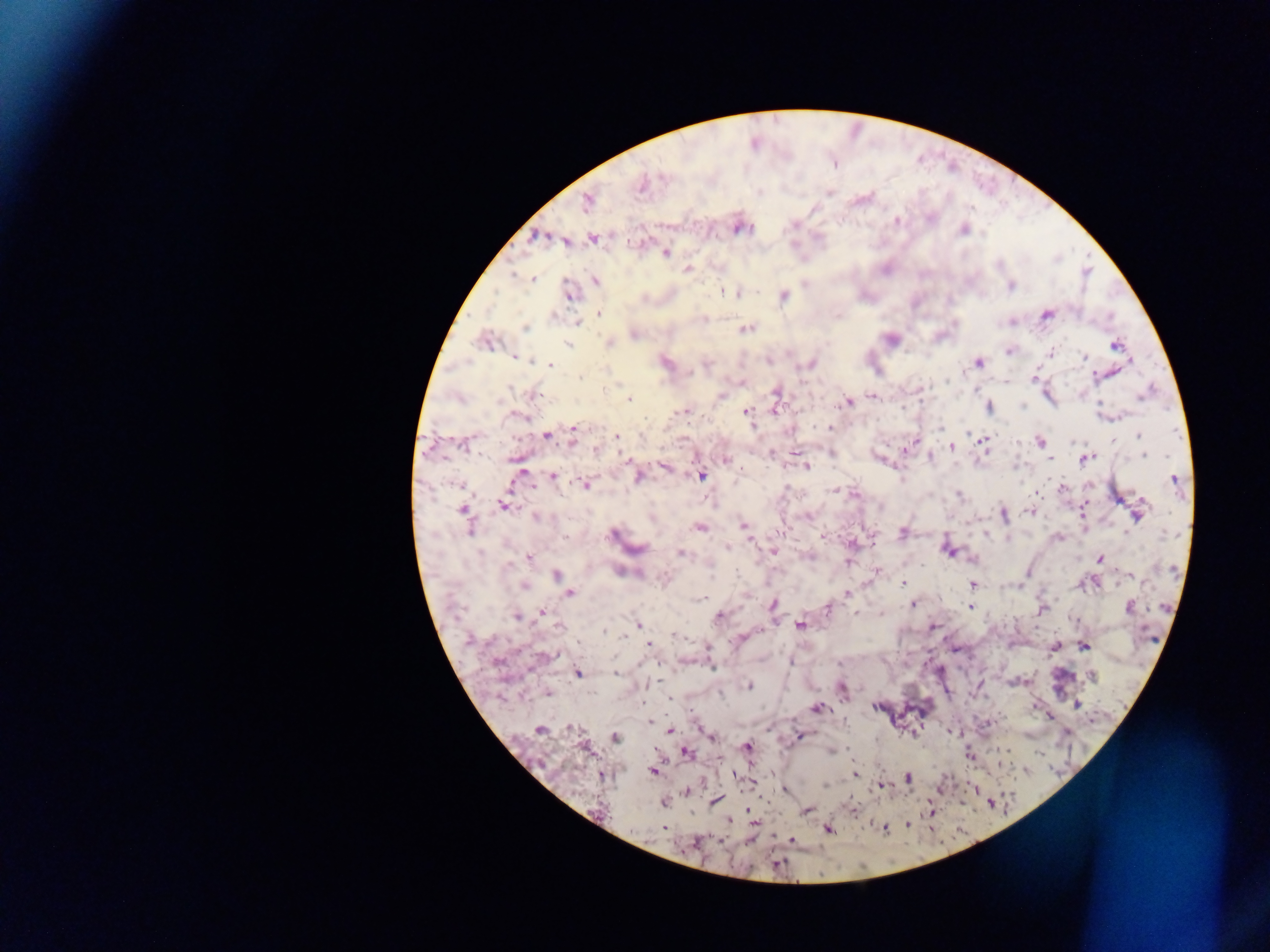
field_of_view: single
country: Ghana
capture: mobile-phone photograph through a microscope
preparation: thick blood smear
plasmodium_parasite_locations: 'approximate centers as (x, y) in pixels: (642, 184), (828, 192), (587, 200), (896, 221), (739, 226), (963, 229), (537, 237), (593, 238), (573, 239), (565, 241), (665, 253), (687, 269), (533, 279), (594, 281), (1010, 286), (569, 292), (737, 293), (782, 295), (598, 314), (1046, 314), (1010, 321), (577, 323), (526, 328), (744, 328), (634, 334), (890, 339), (486, 340), (608, 343), (566, 344), (1115, 345), (1010, 351), (1052, 352), (513, 356), (1084, 359), (664, 361), (977, 362), (810, 364), (551, 365), (1095, 375), (1035, 377), (777, 393), (531, 394), (720, 395), (873, 396), (629, 400), (847, 402), (987, 407), (774, 408), (684, 409), (746, 410), (517, 416), (828, 427), (573, 429), (547, 434), (1140, 434), (573, 437), (616, 438), (982, 440), (1039, 441), (464, 444), (904, 447), (950, 447), (595, 449), (830, 452), (772, 453), (1144, 455), (930, 456), (1085, 458), (726, 459), (806, 465), (665, 467), (520, 472), (701, 474), (637, 475), (552, 476), (1174, 479), (584, 484), (1061, 487), (836, 489), (854, 493), (958, 494), (503, 505), (464, 509), (1083, 509), (1030, 511), (1137, 513), (1002, 514), (808, 515), (537, 516), (653, 518), (744, 526), (700, 527), (470, 528), (902, 532), (613, 533), (822, 535), (986, 536), (1057, 537), (851, 543), (727, 546), (635, 548), (947, 549), (773, 551), (679, 553), (809, 556), (528, 557), (971, 558), (1100, 559), (849, 560), (624, 571), (876, 571), (557, 574), (1131, 575), (562, 581), (903, 582), (971, 584), (523, 586), (569, 592), (847, 593), (701, 599), (913, 604), (773, 605), (971, 606), (827, 607), (1129, 607), (1041, 609), (541, 613), (882, 613), (855, 614), (517, 616), (719, 616), (800, 624), (638, 625), (932, 626), (604, 630), (674, 635), (621, 636), (742, 637), (1083, 644), (649, 645), (1053, 646), (546, 656), (712, 667), (616, 672), (577, 673), (1090, 676), (749, 686), (842, 688), (546, 692), (1076, 703), (875, 706), (816, 708), (1049, 715), (649, 721), (985, 724), (539, 729), (670, 730), (951, 732), (1067, 733), (615, 736), (710, 736), (799, 736), (584, 746), (746, 747), (831, 751), (686, 752), (969, 755), (652, 771), (853, 773), (600, 774), (733, 774), (907, 777), (751, 782), (881, 785), (974, 788), (784, 789), (686, 791), (714, 801), (663, 802), (851, 809), (750, 810), (806, 810), (931, 810), (728, 821), (907, 824), (884, 827), (664, 828), (828, 829), (750, 839), (790, 839), (691, 843)'
image_size: 1270×952 pixels